Report the malaria status of this cell.
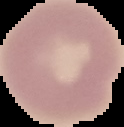
It is uninfected.

Cell region segmented out of the field of view; the surrounding area is masked to black. Image is 124×127 pixels. From a thin blood smear.